Point out each leukocyte.
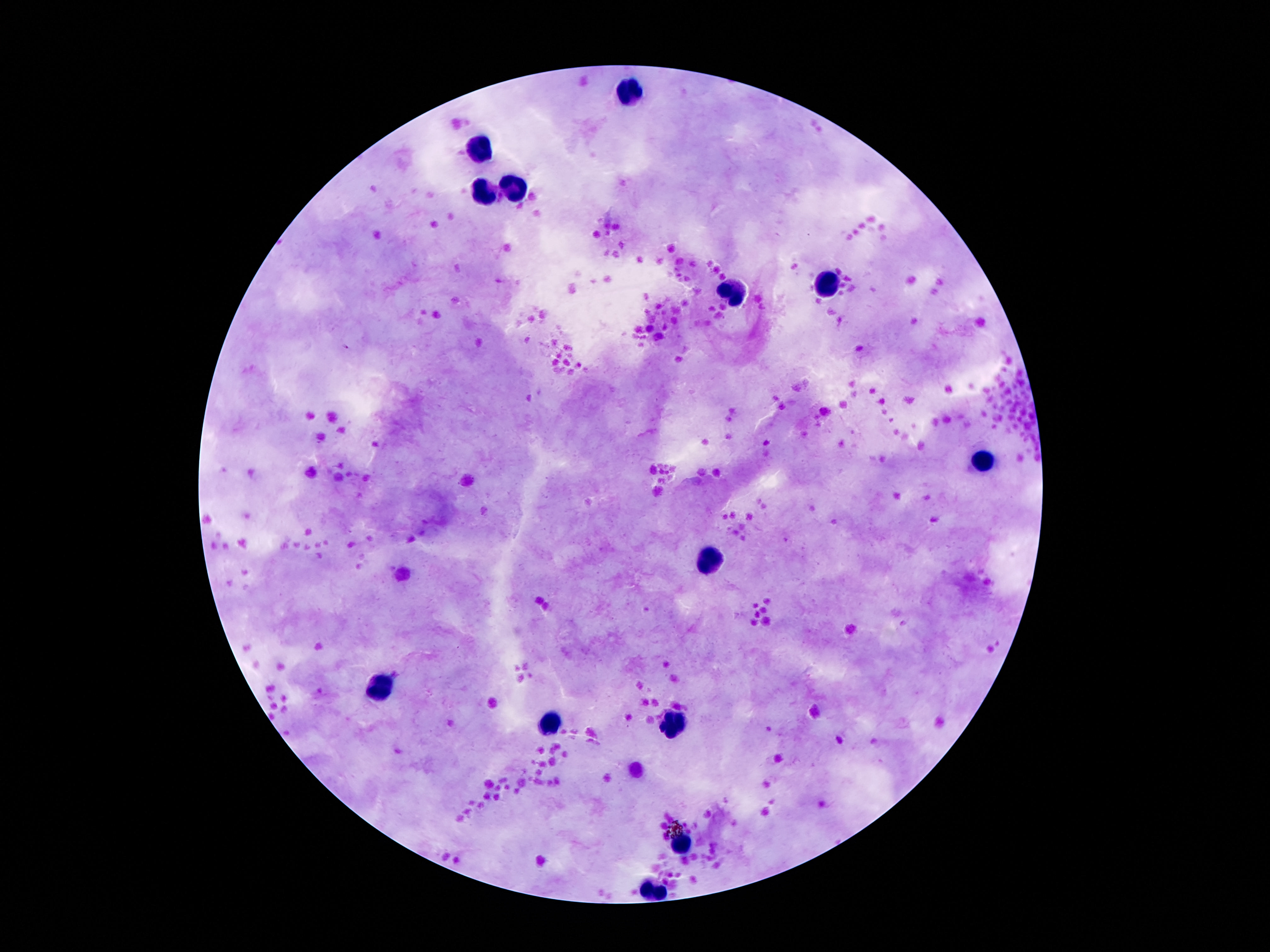

Approximate centers as (x, y) in pixels.
Leukocytes: (626, 93), (483, 146), (517, 190), (487, 195), (826, 287), (733, 291), (983, 459), (710, 560), (380, 688), (551, 723), (674, 727), (681, 843), (653, 892).

Summary:
  - Magnification: 100x
  - Preparation: thick blood film
  - Stain: Giemsa
  - Capture: smartphone camera through the microscope eyepiece
  - Image size: 1270×952 pixels
  - Patient malaria status: uninfected
  - Field of view: single